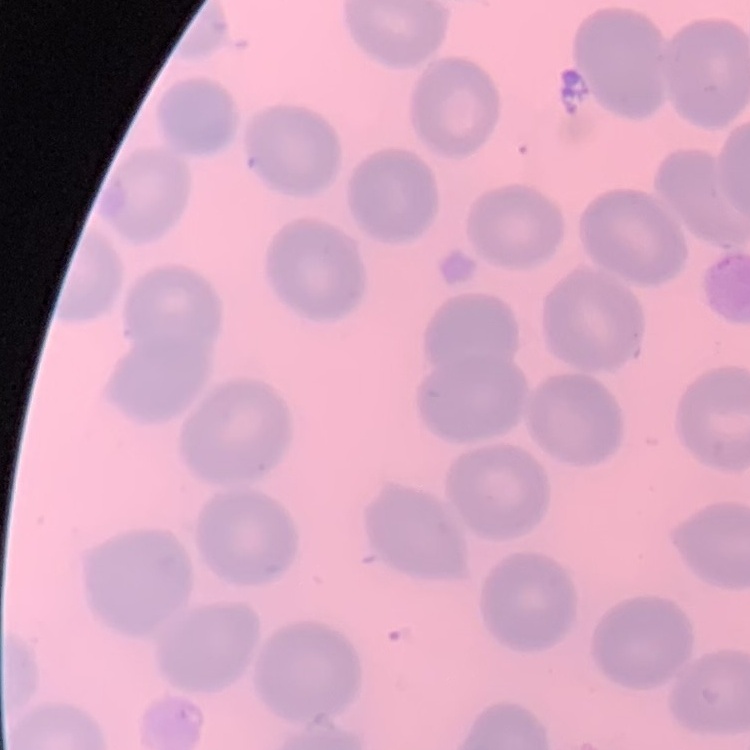
Summary:
  - Erythrocyte morphology: no rouleaux formation
  - Image type: square crop of a larger photomicrograph
  - Stain: Field's or Giemsa
  - Preparation: thin blood film